Outline each blood parasite and name the species.
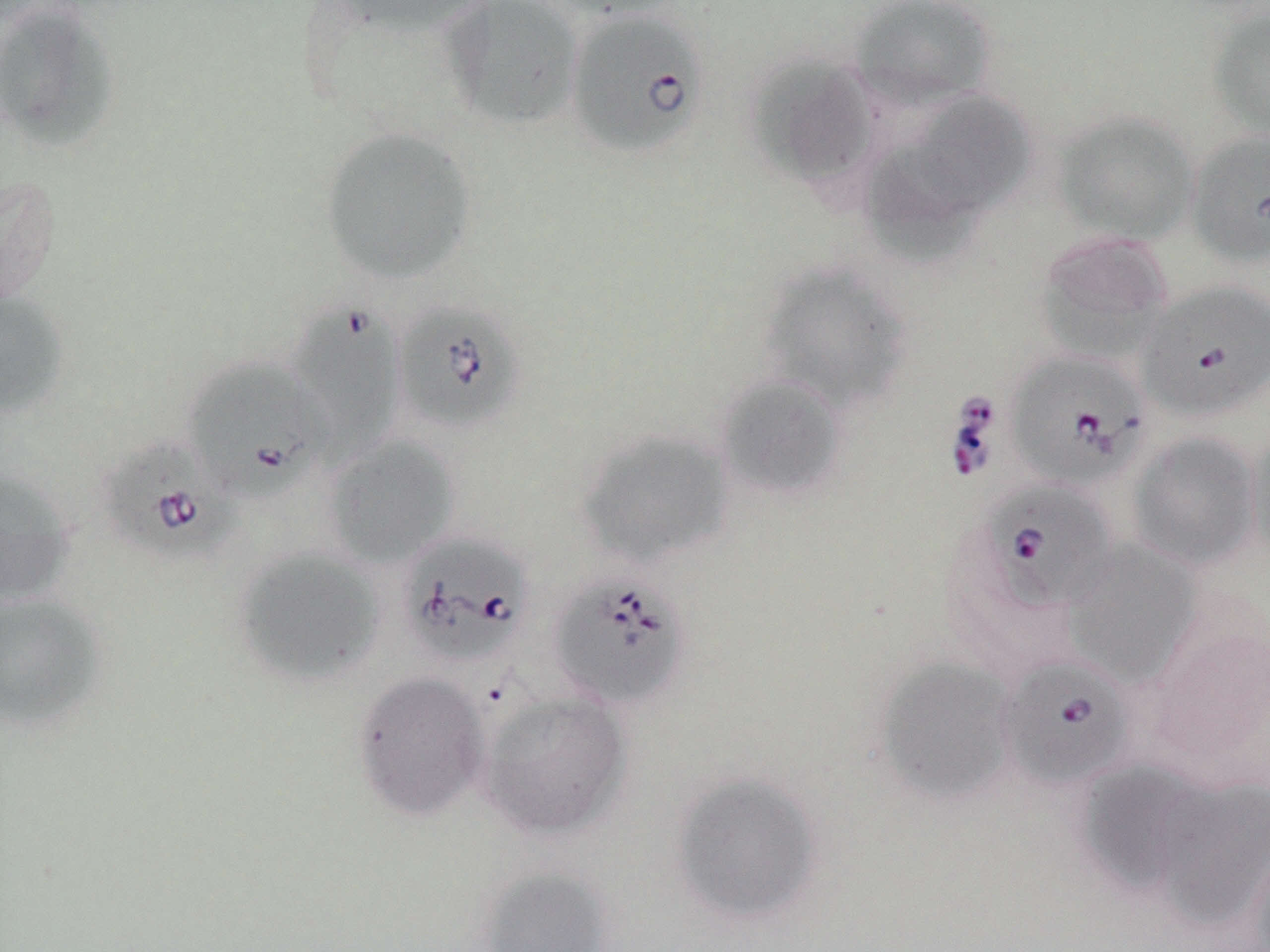
Approximate bounding boxes as named x1/y1/x2/y2 corners in pixels.
Babesia divergens-infected red blood cells: (x1=566, y1=9, x2=709, y2=159), (x1=1188, y1=129, x2=1270, y2=267), (x1=1137, y1=280, x2=1270, y2=422), (x1=392, y1=300, x2=527, y2=433), (x1=287, y1=301, x2=402, y2=460), (x1=1005, y1=350, x2=1151, y2=491), (x1=184, y1=358, x2=327, y2=503), (x1=95, y1=437, x2=239, y2=564), (x1=979, y1=480, x2=1118, y2=612), (x1=398, y1=532, x2=535, y2=667), (x1=548, y1=571, x2=693, y2=710), (x1=997, y1=655, x2=1135, y2=789).
No Plasmodium falciparum, Plasmodium ovale, Plasmodium malariae, Plasmodium vivax, or Trypanosoma brucei observed.

slide-level diagnosis = Babesia divergens
field of view = one of a larger specimen
uninfected red blood cell locations = approximate bounding boxes as named x1/y1/x2/y2 corners in pixels: (x1=320, y1=0, x2=493, y2=36), (x1=545, y1=0, x2=687, y2=20), (x1=849, y1=0, x2=998, y2=111), (x1=440, y1=1, x2=584, y2=131), (x1=0, y1=4, x2=120, y2=153), (x1=1206, y1=5, x2=1270, y2=142), (x1=742, y1=52, x2=880, y2=191), (x1=902, y1=91, x2=1037, y2=216), (x1=1052, y1=111, x2=1199, y2=244), (x1=318, y1=126, x2=478, y2=284), (x1=859, y1=148, x2=982, y2=267), (x1=1, y1=174, x2=61, y2=312), (x1=1032, y1=232, x2=1173, y2=364), (x1=757, y1=261, x2=913, y2=415), (x1=0, y1=289, x2=68, y2=420), (x1=714, y1=374, x2=848, y2=503), (x1=1245, y1=425, x2=1270, y2=566), (x1=576, y1=428, x2=735, y2=568), (x1=1127, y1=431, x2=1262, y2=571), (x1=322, y1=435, x2=460, y2=567), (x1=0, y1=468, x2=76, y2=607), (x1=1062, y1=540, x2=1203, y2=686), (x1=232, y1=546, x2=386, y2=687), (x1=0, y1=592, x2=108, y2=733), (x1=874, y1=657, x2=1020, y2=806), (x1=352, y1=670, x2=490, y2=822), (x1=478, y1=692, x2=632, y2=840), (x1=1077, y1=761, x2=1202, y2=899), (x1=669, y1=770, x2=825, y2=929), (x1=1152, y1=776, x2=1270, y2=931), (x1=1246, y1=819, x2=1270, y2=952), (x1=473, y1=866, x2=618, y2=952)
image size = 1270×952 pixels
preparation = thin blood smear
magnification = 1000x
modality = light microscopy
stain = May-Grünwald-Giemsa